Assess for Plasmodium parasites.
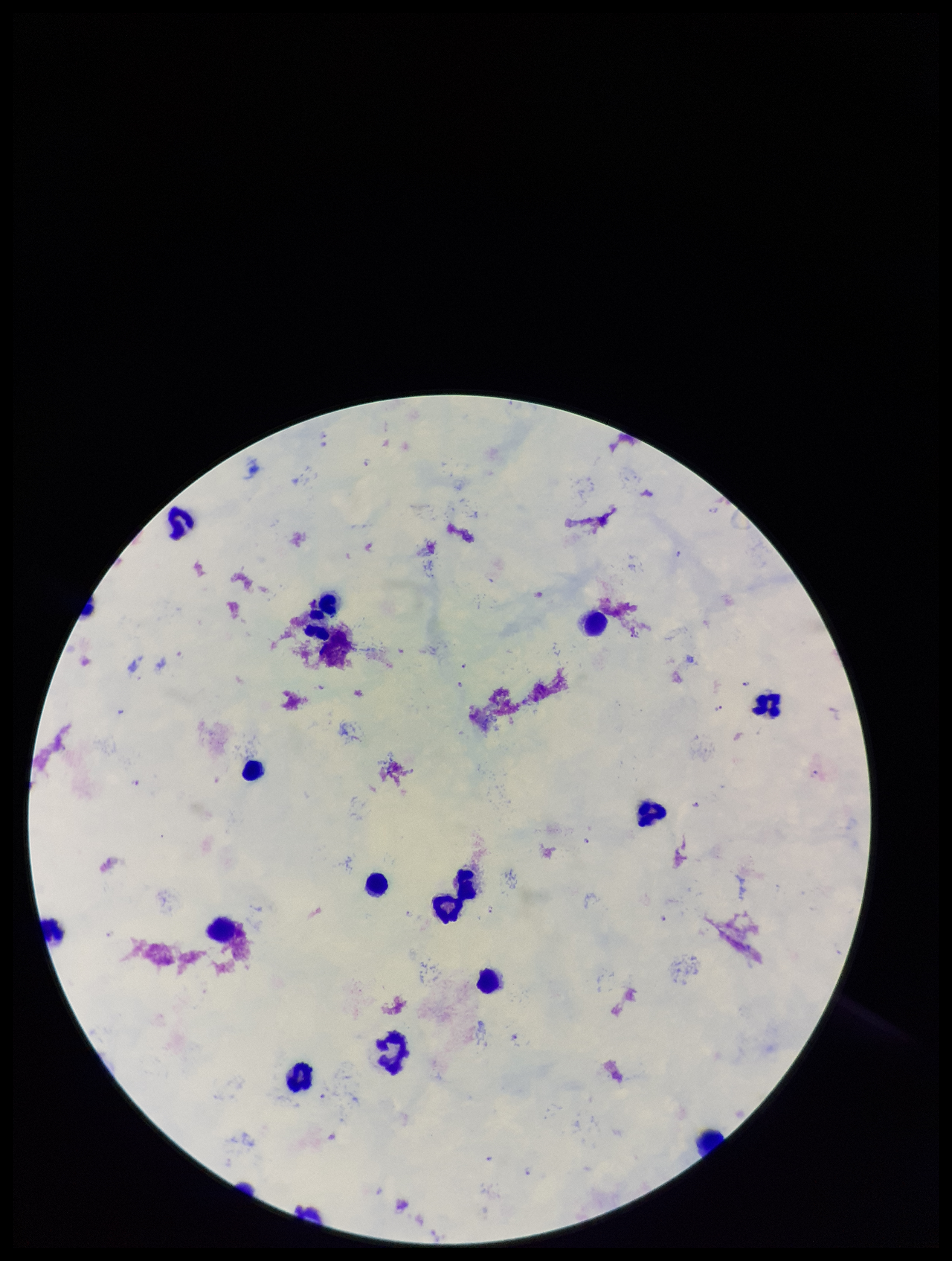

Detected.

Leukocyte count: 15. Single field of view. Stained with Giemsa. Parasite count: 11. Photographed through the microscope eyepiece with a smartphone camera. Species reported for this patient: Plasmodium falciparum. Image is 952×1261 pixels. Preparation: thick smear. Patient malaria status: infected.